Identify the cell.
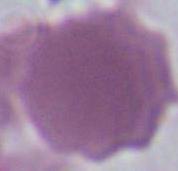

An erythrocyte.

Summary:
  - Modality: photomicrograph
  - Magnification: 1000x